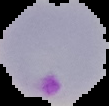
Summary:
  - Malaria status: parasitized
  - Image size: 109×106 pixels
  - Image type: segmented cell region with the area outside set to black
  - Preparation: thin blood smear